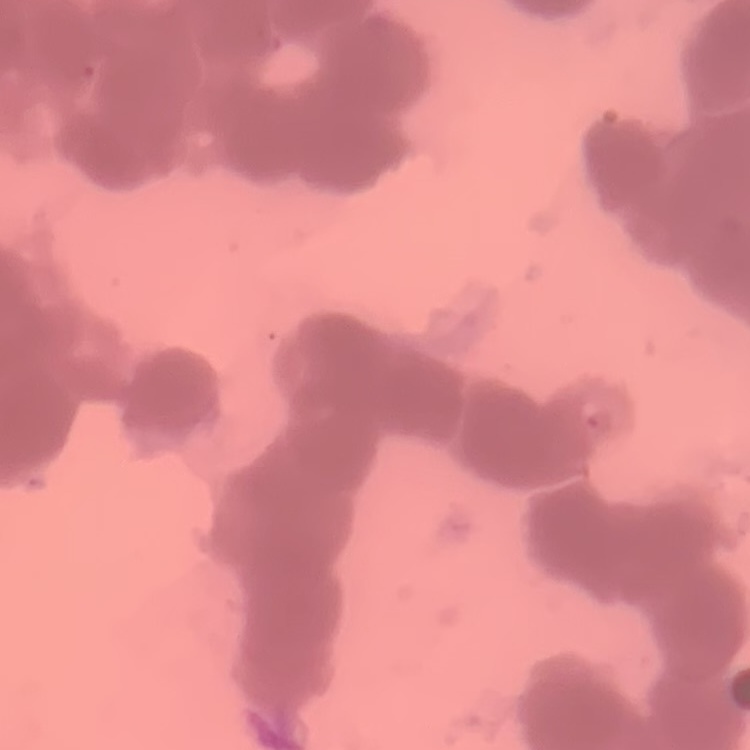
erythrocyte_morphology: rouleaux formation
preparation: thin blood smear
stain: Field's or Giemsa
image_type: square crop of a larger photomicrograph